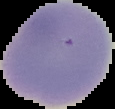

preparation = thin blood film
result = negative for Plasmodium parasites
image type = segmented cell region with the area outside set to black
image size = 115×109 pixels